Name the parasite shown.
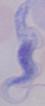

A trypanosome.

Summary:
  - Modality: micrograph
  - Magnification: 1000x